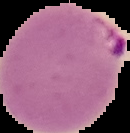

image size = 130×133 pixels
image type = segmented cell region with the area outside set to black
preparation = thin blood smear
malaria status = parasitized